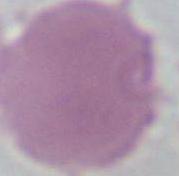

1000x magnification. Photomicrograph. An erythrocyte is shown.